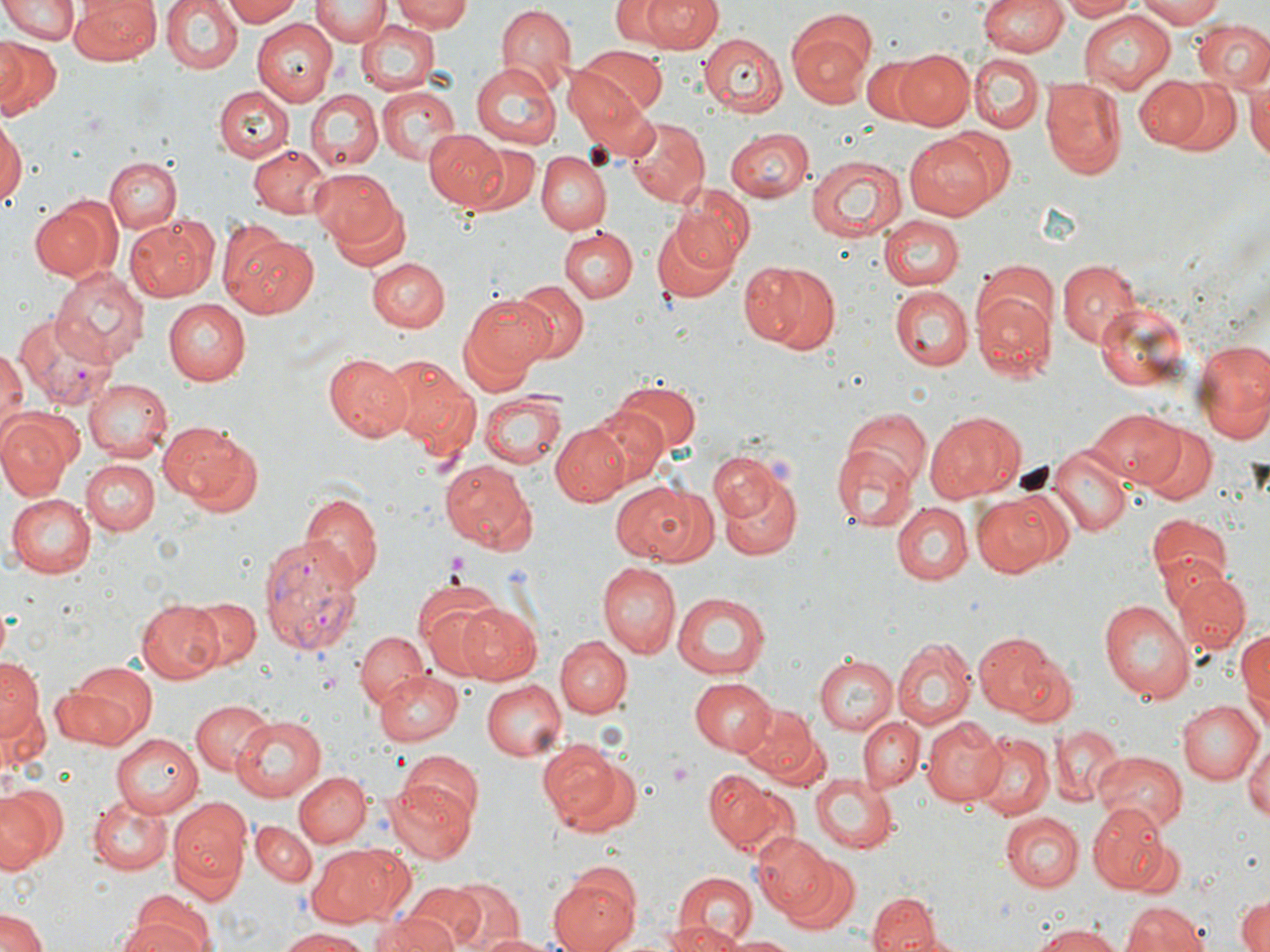

Approximate bounding boxes as named x1/y1/x2/y2 corners in pixels. Platelet locations: (x1=445, y1=550, x2=471, y2=579), (x1=669, y1=757, x2=696, y2=789). Plasmodium vivax-infected red blood cell locations: (x1=13, y1=311, x2=112, y2=410), (x1=256, y1=534, x2=363, y2=653). Uninfected red blood cell locations: (x1=161, y1=0, x2=242, y2=76), (x1=224, y1=0, x2=304, y2=26), (x1=313, y1=0, x2=388, y2=45), (x1=393, y1=0, x2=477, y2=33), (x1=614, y1=0, x2=667, y2=44), (x1=637, y1=0, x2=722, y2=54), (x1=979, y1=0, x2=1066, y2=58), (x1=1058, y1=0, x2=1138, y2=21), (x1=1139, y1=0, x2=1228, y2=26), (x1=0, y1=1, x2=80, y2=45), (x1=73, y1=1, x2=160, y2=63), (x1=495, y1=5, x2=574, y2=90), (x1=1079, y1=10, x2=1179, y2=93), (x1=357, y1=18, x2=440, y2=96), (x1=251, y1=19, x2=336, y2=106), (x1=788, y1=20, x2=876, y2=102), (x1=1193, y1=20, x2=1270, y2=91), (x1=697, y1=31, x2=787, y2=115), (x1=0, y1=37, x2=29, y2=110), (x1=0, y1=37, x2=62, y2=119), (x1=569, y1=49, x2=663, y2=127), (x1=894, y1=50, x2=975, y2=130), (x1=969, y1=55, x2=1044, y2=134), (x1=862, y1=57, x2=930, y2=124), (x1=471, y1=62, x2=562, y2=148), (x1=1134, y1=76, x2=1207, y2=148), (x1=1159, y1=76, x2=1241, y2=156), (x1=1247, y1=76, x2=1270, y2=168), (x1=569, y1=79, x2=657, y2=166), (x1=1041, y1=79, x2=1127, y2=179), (x1=213, y1=86, x2=293, y2=162), (x1=376, y1=86, x2=462, y2=168), (x1=303, y1=90, x2=382, y2=172), (x1=0, y1=118, x2=24, y2=210), (x1=628, y1=120, x2=707, y2=206), (x1=724, y1=127, x2=813, y2=202), (x1=936, y1=129, x2=1015, y2=207), (x1=425, y1=130, x2=511, y2=211), (x1=905, y1=135, x2=996, y2=222), (x1=464, y1=143, x2=541, y2=216), (x1=249, y1=144, x2=330, y2=218), (x1=538, y1=151, x2=611, y2=235), (x1=806, y1=154, x2=906, y2=244), (x1=104, y1=157, x2=180, y2=232), (x1=310, y1=169, x2=402, y2=252), (x1=673, y1=185, x2=756, y2=269), (x1=29, y1=197, x2=119, y2=281), (x1=329, y1=200, x2=411, y2=272), (x1=878, y1=215, x2=963, y2=290), (x1=126, y1=217, x2=215, y2=303), (x1=652, y1=217, x2=738, y2=304), (x1=558, y1=227, x2=637, y2=303), (x1=226, y1=234, x2=319, y2=319), (x1=365, y1=257, x2=447, y2=332), (x1=1056, y1=260, x2=1140, y2=346), (x1=744, y1=261, x2=839, y2=354), (x1=972, y1=261, x2=1057, y2=337), (x1=49, y1=268, x2=146, y2=368), (x1=510, y1=281, x2=588, y2=361), (x1=888, y1=284, x2=972, y2=370), (x1=973, y1=293, x2=1054, y2=379), (x1=462, y1=294, x2=553, y2=385), (x1=166, y1=298, x2=252, y2=386), (x1=1092, y1=299, x2=1195, y2=395), (x1=1194, y1=336, x2=1270, y2=447), (x1=0, y1=348, x2=25, y2=438), (x1=325, y1=353, x2=417, y2=444), (x1=383, y1=357, x2=480, y2=451), (x1=82, y1=378, x2=171, y2=462), (x1=610, y1=382, x2=701, y2=459), (x1=479, y1=390, x2=568, y2=470), (x1=583, y1=404, x2=669, y2=489), (x1=1088, y1=407, x2=1182, y2=487), (x1=843, y1=409, x2=930, y2=491), (x1=0, y1=411, x2=78, y2=497), (x1=925, y1=411, x2=1024, y2=502), (x1=157, y1=419, x2=258, y2=511), (x1=551, y1=421, x2=634, y2=504), (x1=1139, y1=424, x2=1216, y2=503), (x1=1047, y1=442, x2=1132, y2=538), (x1=831, y1=446, x2=918, y2=535), (x1=707, y1=451, x2=784, y2=525), (x1=81, y1=459, x2=158, y2=534), (x1=439, y1=462, x2=535, y2=553), (x1=717, y1=470, x2=804, y2=560), (x1=609, y1=481, x2=710, y2=565), (x1=969, y1=488, x2=1069, y2=577), (x1=299, y1=491, x2=382, y2=590), (x1=7, y1=493, x2=97, y2=578), (x1=891, y1=502, x2=973, y2=585), (x1=1145, y1=512, x2=1231, y2=597), (x1=598, y1=562, x2=680, y2=659), (x1=1172, y1=572, x2=1252, y2=655), (x1=416, y1=590, x2=509, y2=679), (x1=671, y1=591, x2=774, y2=680), (x1=181, y1=594, x2=261, y2=670), (x1=1097, y1=599, x2=1195, y2=705), (x1=136, y1=600, x2=222, y2=682), (x1=455, y1=600, x2=544, y2=686), (x1=1236, y1=625, x2=1270, y2=734), (x1=355, y1=629, x2=428, y2=712), (x1=974, y1=631, x2=1063, y2=719), (x1=556, y1=636, x2=631, y2=717), (x1=892, y1=636, x2=975, y2=731), (x1=1004, y1=649, x2=1077, y2=727), (x1=813, y1=656, x2=898, y2=735), (x1=1, y1=657, x2=42, y2=736), (x1=56, y1=665, x2=156, y2=749), (x1=372, y1=670, x2=463, y2=745), (x1=688, y1=677, x2=774, y2=757), (x1=484, y1=680, x2=567, y2=761), (x1=1, y1=699, x2=47, y2=774), (x1=191, y1=699, x2=274, y2=775), (x1=1176, y1=699, x2=1263, y2=785), (x1=737, y1=703, x2=819, y2=779), (x1=230, y1=714, x2=328, y2=803), (x1=859, y1=716, x2=924, y2=793), (x1=921, y1=716, x2=1005, y2=806), (x1=1052, y1=723, x2=1124, y2=806), (x1=113, y1=733, x2=204, y2=817), (x1=971, y1=733, x2=1055, y2=818), (x1=1243, y1=735, x2=1270, y2=826), (x1=538, y1=738, x2=636, y2=839), (x1=399, y1=752, x2=484, y2=831), (x1=1092, y1=752, x2=1186, y2=831), (x1=705, y1=770, x2=779, y2=849), (x1=295, y1=771, x2=368, y2=848), (x1=810, y1=774, x2=900, y2=852), (x1=381, y1=780, x2=477, y2=865), (x1=0, y1=784, x2=65, y2=874), (x1=89, y1=794, x2=171, y2=872), (x1=168, y1=800, x2=253, y2=899), (x1=1089, y1=804, x2=1166, y2=893), (x1=1000, y1=811, x2=1083, y2=893), (x1=250, y1=818, x2=317, y2=888), (x1=753, y1=834, x2=830, y2=917), (x1=1125, y1=834, x2=1184, y2=897), (x1=305, y1=846, x2=406, y2=924), (x1=779, y1=854, x2=858, y2=933), (x1=549, y1=871, x2=643, y2=952), (x1=668, y1=872, x2=762, y2=951), (x1=444, y1=880, x2=524, y2=952), (x1=406, y1=882, x2=487, y2=949), (x1=867, y1=894, x2=937, y2=952), (x1=1235, y1=894, x2=1270, y2=952), (x1=1120, y1=900, x2=1210, y2=952), (x1=120, y1=903, x2=212, y2=952), (x1=0, y1=909, x2=48, y2=952), (x1=370, y1=913, x2=455, y2=952), (x1=659, y1=922, x2=747, y2=952), (x1=1032, y1=923, x2=1123, y2=952), (x1=896, y1=924, x2=973, y2=952), (x1=279, y1=928, x2=376, y2=951), (x1=471, y1=932, x2=567, y2=952), (x1=723, y1=934, x2=799, y2=952). Slide-level diagnosis: Plasmodium vivax. 1000x magnification. Light microscopy. Image is 1270×952 pixels. May-Grünwald-Giemsa-stained preparation. One field of a larger specimen. Thin blood film.